Point out each leukocyte.
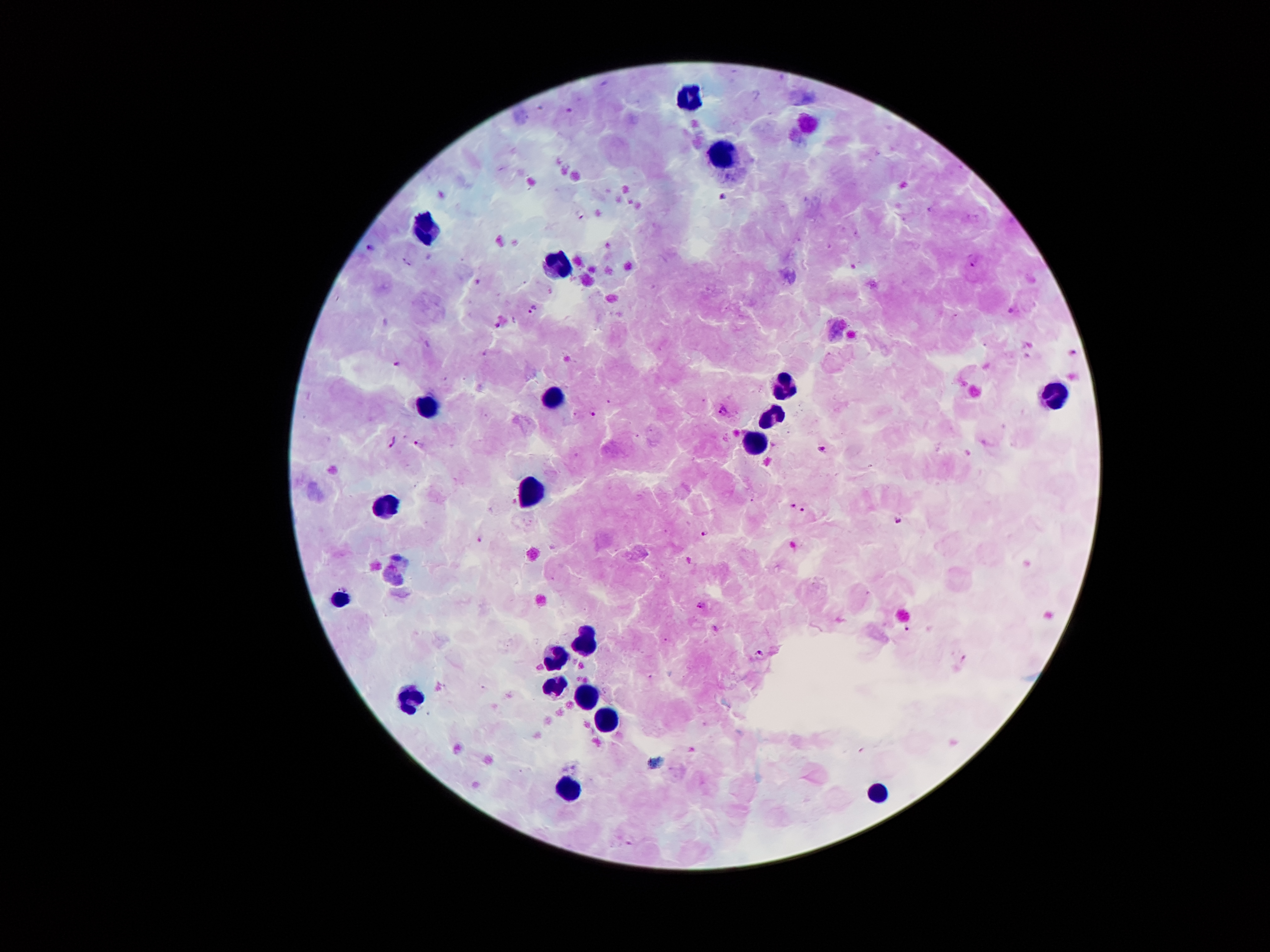

Approximate centers as {x, y} in pixels.
Leukocytes: {693, 96}, {722, 155}, {425, 226}, {559, 264}, {786, 384}, {558, 392}, {1058, 392}, {426, 403}, {774, 420}, {754, 447}, {532, 491}, {384, 504}, {338, 599}, {584, 641}, {557, 657}, {552, 689}, {401, 695}, {586, 697}, {608, 718}, {568, 785}, {879, 795}.

Plasmodium parasite locations: {570, 110}, {725, 197}, {928, 208}, {581, 214}, {370, 246}, {976, 260}, {532, 307}, {398, 364}, {723, 409}, {594, 413}, {391, 440}, {419, 443}, {821, 449}, {792, 506}, {803, 511}, {898, 519}, {704, 533}, {480, 538}, {700, 605}, {906, 630}, {760, 651}. Thick peripheral-blood smear. 100x magnification. Giemsa-stained preparation. Patient malaria status: positive for Plasmodium falciparum. One field from this slide. Photographed through the microscope eyepiece with a smartphone camera. Image is 1270×952 pixels.